Give the extent of all Trypanosoma brucei.
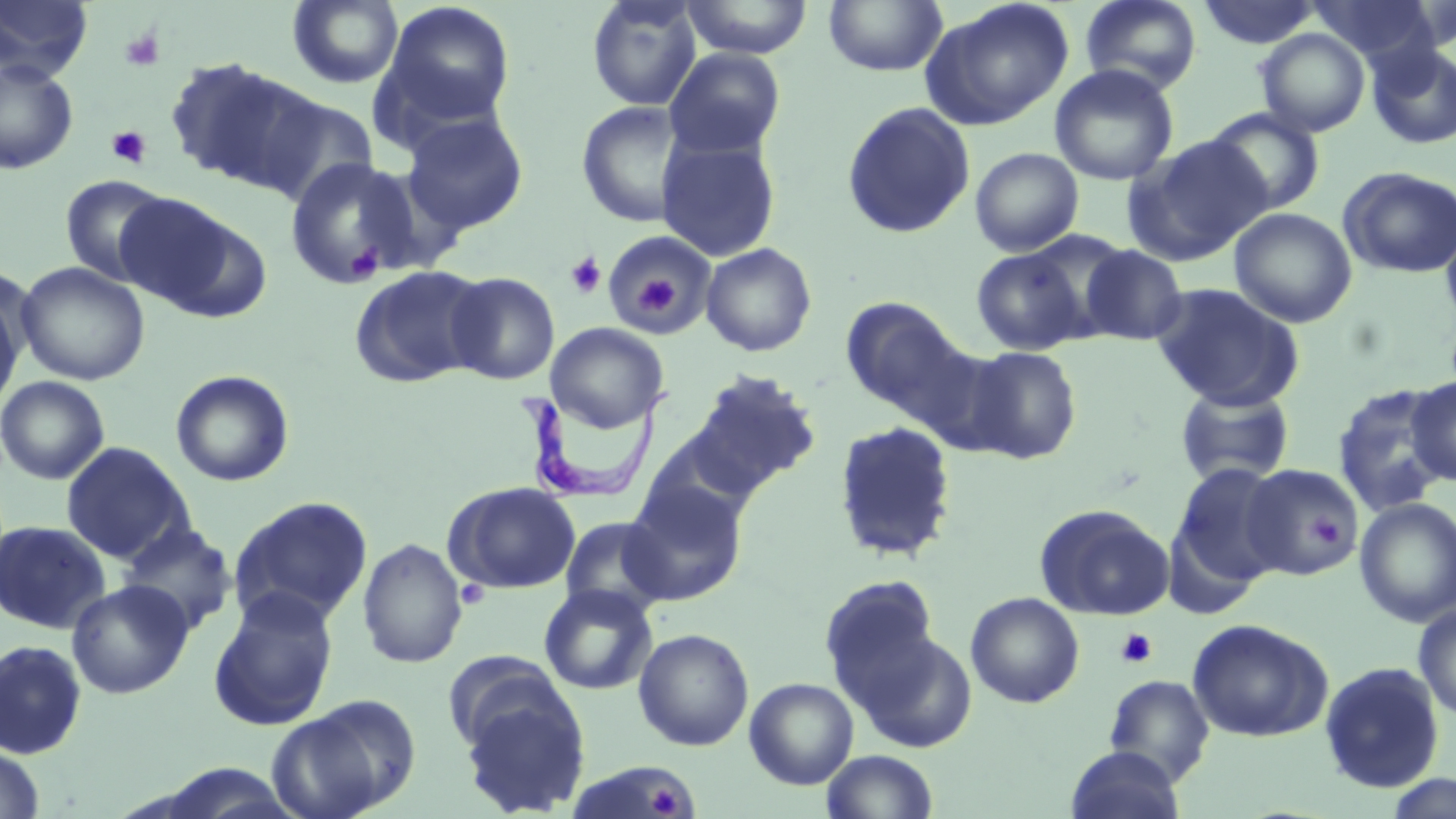
Approximate bounding boxes as (x1,y1)-(x2,y2) corner pairs in pixels.
Trypanosoma brucei: (526,390)-(672,504).

slide-level diagnosis = Trypanosoma brucei
stain = May-Grünwald-Giemsa
field of view = single
preparation = thin blood smear
platelet locations = approximate bounding boxes as (x1,y1)-(x2,y2) corner pairs in pixels: (119,28)-(165,71), (106,126)-(153,168), (344,241)-(383,285), (565,252)-(607,299), (624,261)-(694,320), (1308,514)-(1345,549), (456,580)-(488,609), (1115,628)-(1158,669), (645,782)-(690,817)
uninfected red blood cell locations = approximate bounding boxes as (x1,y1)-(x2,y2) corner pairs in pixels: (288,0)-(404,89), (586,0)-(704,111), (680,0)-(814,59), (823,0)-(947,76), (920,0)-(1075,131), (1079,0)-(1202,94), (1309,0)-(1441,64), (0,1)-(93,82), (381,1)-(516,129), (1198,1)-(1322,49), (1255,28)-(1370,137), (1366,42)-(1456,150), (664,47)-(786,160), (163,56)-(317,192), (0,59)-(78,174), (1049,63)-(1179,186), (252,91)-(379,204), (576,100)-(692,228), (840,102)-(976,238), (1204,107)-(1326,216), (402,111)-(529,234), (656,135)-(781,262), (1123,135)-(1272,267), (969,147)-(1084,257), (285,157)-(423,286), (1339,167)-(1456,278), (59,174)-(173,288), (113,194)-(245,314), (1229,207)-(1357,328), (1440,218)-(1456,332), (603,230)-(716,336), (1019,230)-(1136,338), (701,243)-(817,356), (1079,244)-(1188,346), (971,247)-(1087,355), (16,261)-(150,386), (349,264)-(490,388), (445,272)-(560,385), (1150,283)-(1305,411), (0,285)-(25,418), (841,297)-(973,420), (546,322)-(670,432), (963,345)-(1082,464), (684,369)-(822,499), (170,370)-(294,487), (0,376)-(109,485), (1406,376)-(1456,485), (1333,384)-(1451,516), (1175,385)-(1294,487), (832,420)-(959,564), (639,430)-(765,537), (60,441)-(193,563), (1170,463)-(1289,584), (1241,464)-(1364,579), (621,481)-(749,605), (445,482)-(581,594), (229,495)-(374,628), (1354,497)-(1456,628), (1034,504)-(1175,619), (560,515)-(671,618), (0,520)-(111,634), (117,521)-(237,635), (357,537)-(468,669), (819,574)-(942,704), (66,580)-(194,699), (538,583)-(658,696), (207,588)-(340,731), (965,592)-(1084,709), (1413,604)-(1456,722), (1187,618)-(1332,741), (633,628)-(754,751), (854,630)-(979,754), (0,639)-(87,760), (443,653)-(570,759), (1318,661)-(1445,794), (1104,674)-(1215,785), (744,677)-(859,789), (456,683)-(591,817), (267,697)-(417,819), (0,744)-(45,818), (1066,745)-(1186,819), (820,749)-(939,819), (1383,773)-(1456,819)
image size = 1456×819 pixels
magnification = 1000x
modality = light microscopy